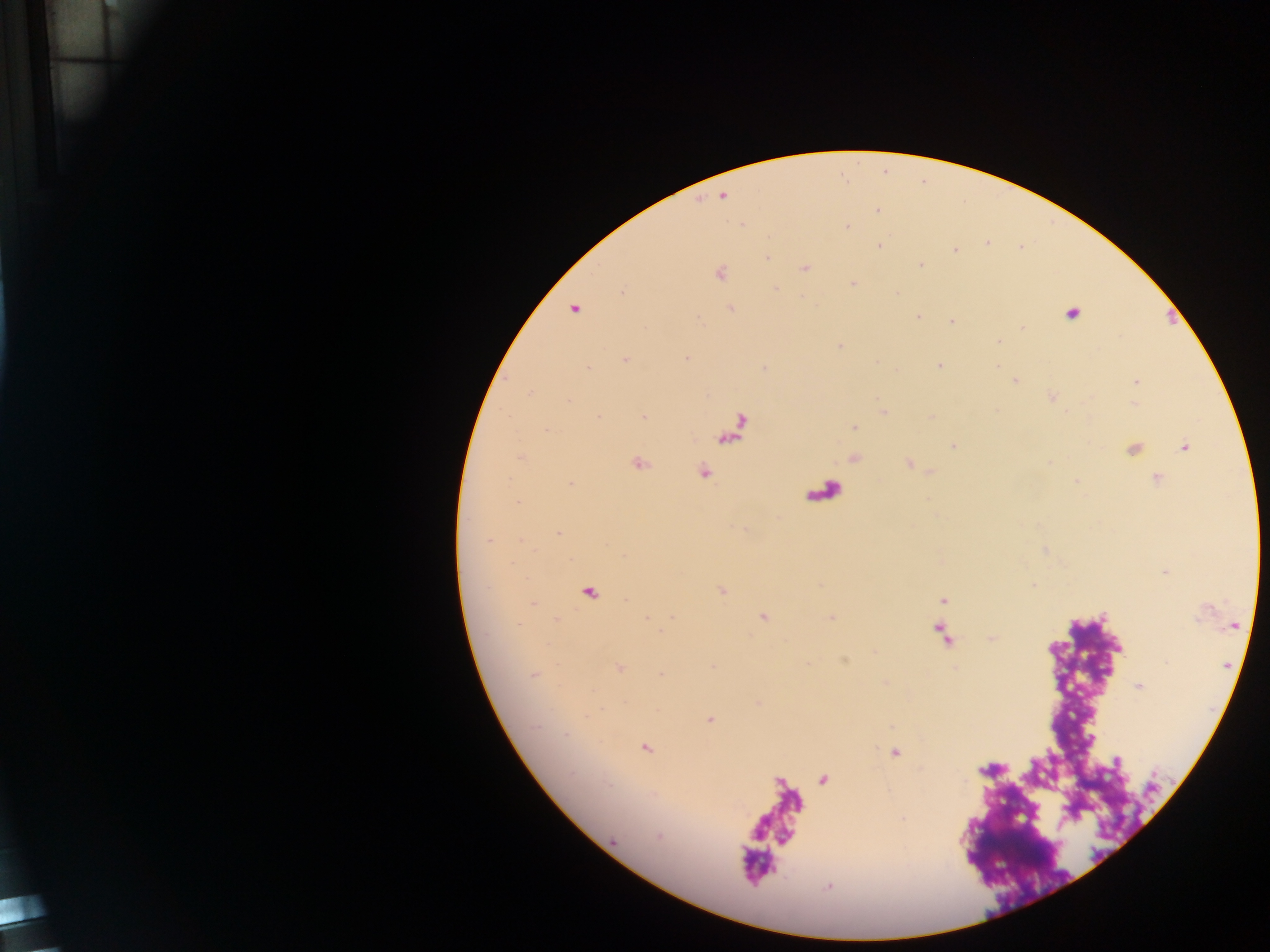
{
  "field_of_view": "single",
  "preparation": "thick blood film",
  "plasmodium_parasite_locations": "approximate centers as {x, y} in pixels: {722, 196}, {877, 211}, {847, 227}, {768, 237}, {879, 245}, {955, 250}, {766, 257}, {920, 264}, {805, 268}, {720, 274}, {853, 284}, {775, 289}, {731, 308}, {574, 309}, {1072, 313}, {919, 316}, {952, 321}, {1023, 327}, {839, 346}, {685, 358}, {625, 359}, {938, 366}, {588, 368}, {1015, 381}, {1137, 381}, {884, 413}, {644, 417}, {855, 427}, {954, 446}, {1185, 447}, {520, 457}, {639, 463}, {704, 471}, {1156, 477}, {1077, 482}, {571, 483}, {518, 502}, {558, 532}, {488, 540}, {942, 600}, {533, 603}, {646, 618}, {763, 618}, {831, 618}, {557, 619}, {519, 624}, {941, 633}, {620, 668}, {534, 674}, {662, 675}, {1139, 686}, {587, 717}, {710, 719}, {566, 735}, {646, 748}, {894, 752}, {903, 818}, {613, 841}",
  "capture": "mobile-phone photograph through a microscope",
  "image_size": "1270×952 pixels",
  "country": "Ghana"
}